Comment on the morphology of the red blood cells.
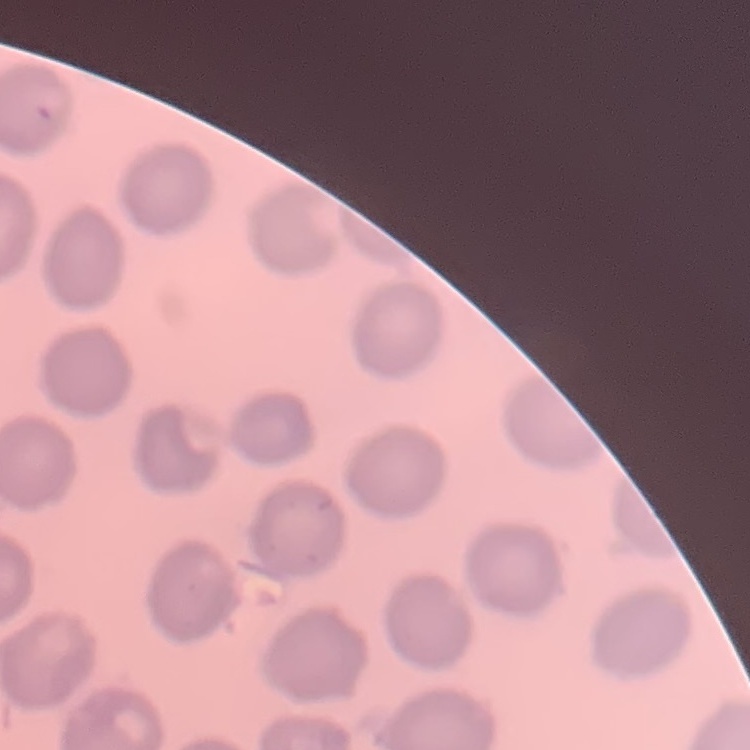

No rouleaux formation.

Summary:
  - Image type: square crop of a larger photomicrograph
  - Preparation: thin blood film
  - Stain: Field's or Giemsa